Find the red blood cells and label each as P. falciparum-infected, uninfected, or of indeterminate infection status.
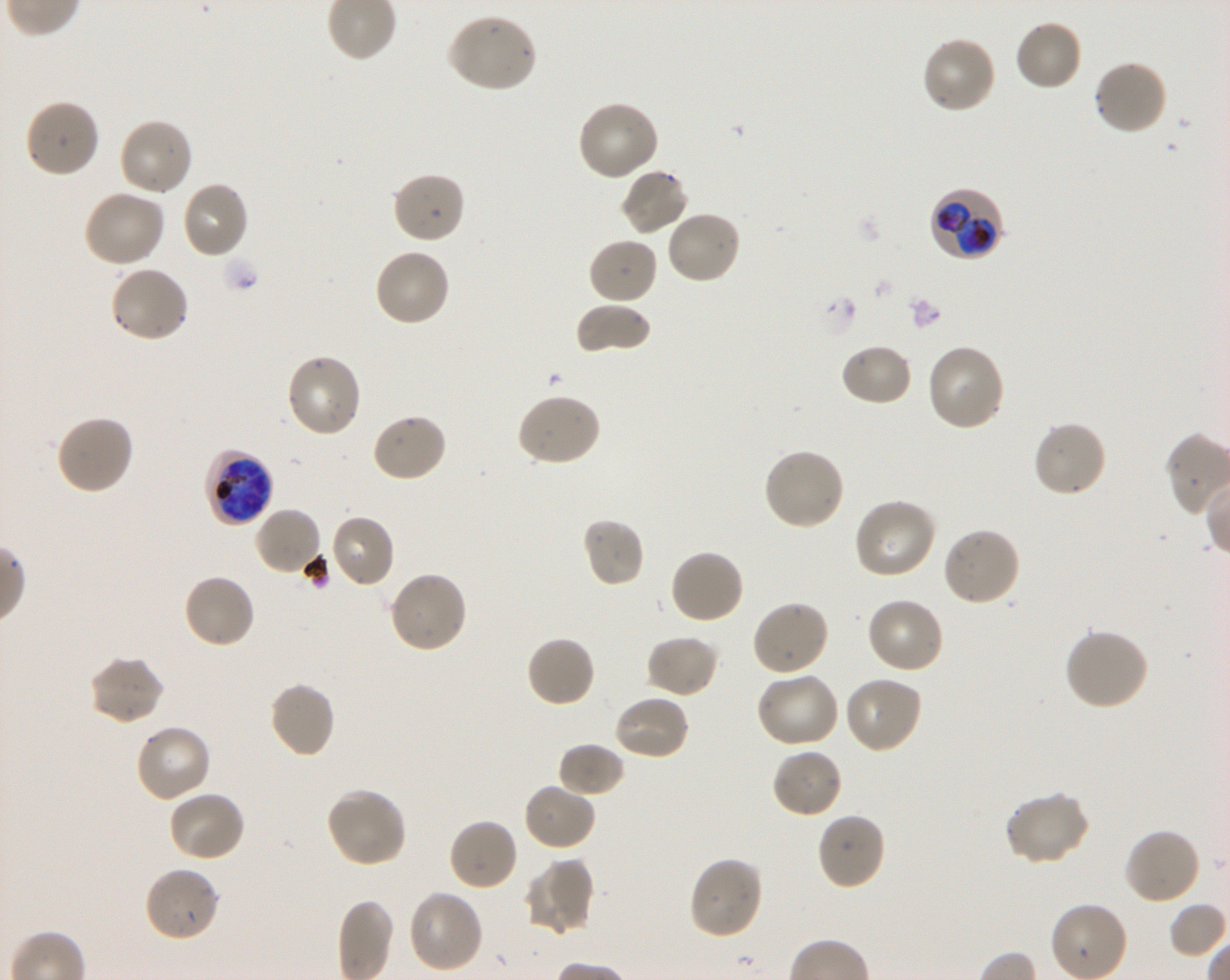
Approximate bounding boxes as (x1, y1, x2, y2) in pixels. Not every red blood cell is marked. A life-cycle stage — or a range of stages, where the recorded stages span more than one — follows each staged infected red blood cell.
Infected red blood cells: (928, 186, 1004, 262) trophozoite; (203, 448, 274, 526) late trophozoite to late schizont.
Uninfected red blood cells: (446, 13, 539, 94), (1013, 18, 1083, 92), (919, 34, 997, 115), (1092, 59, 1169, 138), (24, 98, 101, 179), (577, 101, 660, 182), (118, 117, 194, 198), (619, 168, 690, 237), (391, 170, 466, 245), (181, 180, 249, 259), (82, 190, 165, 268), (665, 209, 742, 285), (587, 236, 659, 306), (372, 248, 451, 328), (109, 265, 190, 344), (575, 302, 652, 355), (839, 343, 914, 408), (925, 344, 1006, 432), (285, 353, 363, 439), (516, 393, 602, 468), (370, 412, 448, 483), (55, 414, 135, 496), (1032, 419, 1108, 499), (762, 447, 847, 532), (853, 497, 937, 580), (253, 506, 324, 577), (329, 514, 396, 589), (581, 517, 645, 587), (941, 525, 1021, 608), (669, 548, 746, 625), (387, 570, 468, 654), (182, 573, 257, 650), (865, 596, 946, 674), (750, 599, 830, 677), (1062, 628, 1150, 711), (644, 634, 719, 699), (525, 635, 597, 708), (87, 655, 164, 726), (756, 671, 841, 748), (843, 675, 923, 754), (268, 680, 336, 759), (612, 694, 691, 761), (133, 723, 212, 803), (557, 743, 626, 799), (771, 747, 845, 819), (522, 782, 597, 852), (326, 787, 409, 868), (167, 790, 247, 862), (1003, 790, 1090, 866), (815, 811, 886, 891), (447, 818, 519, 892), (1123, 827, 1201, 906), (687, 855, 764, 940), (522, 858, 594, 936), (143, 866, 222, 943), (405, 888, 485, 975).
No red blood cells of indeterminate infection status observed.

Shaking in-vitro culture of P. falciparum strain 3D7. Giemsa-stained preparation. One field from this slide. 100x oil-immersion objective, numerical aperture 1.30. Blood group of the donor: O+. Image is 1230×980 pixels. Thin blood smear.